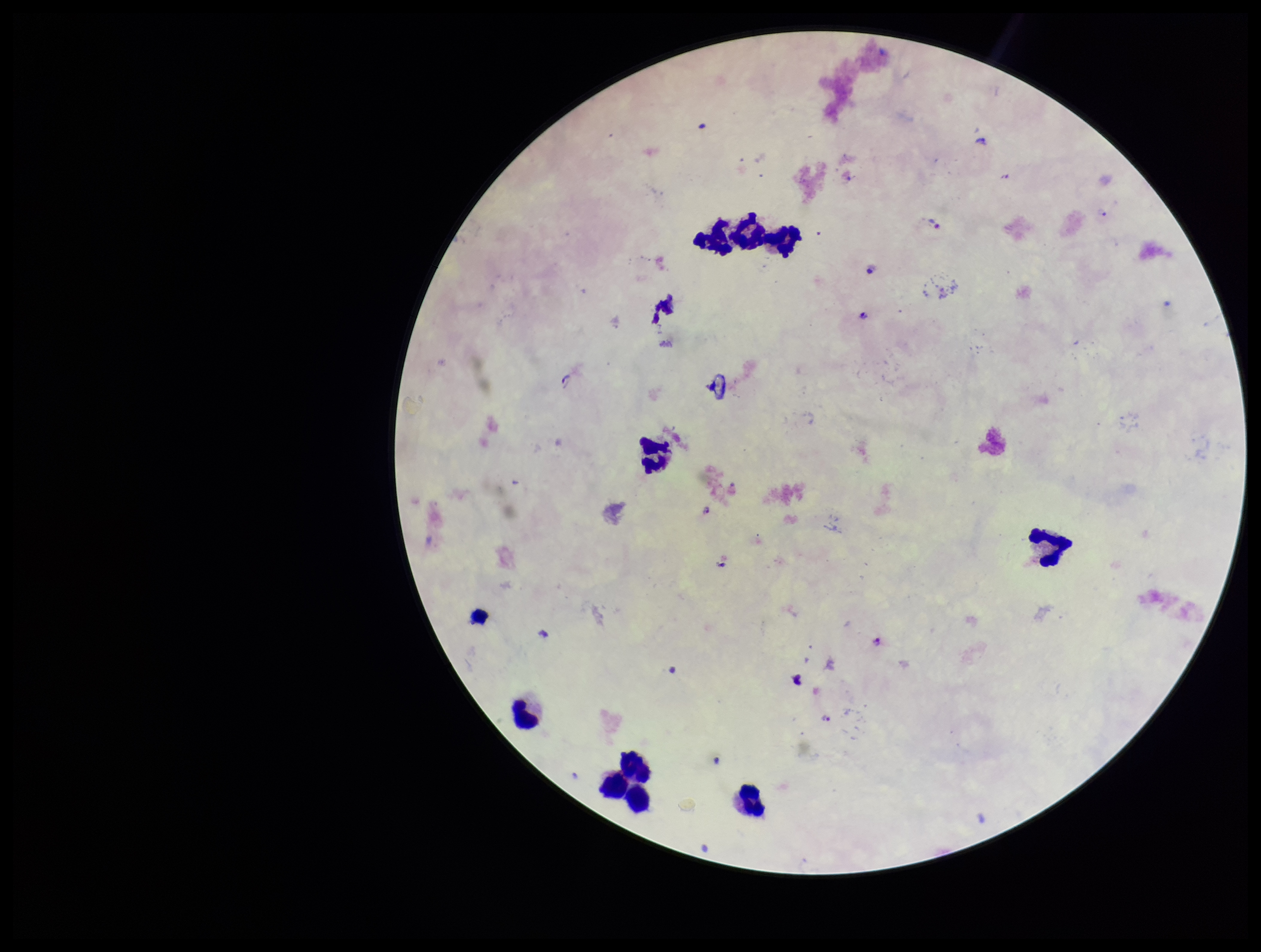

Summary:
  - Stain: Giemsa
  - Capture: smartphone photograph through the microscope eyepiece
  - Plasmodium parasites: detected
  - Species reported for this patient: Plasmodium falciparum
  - Preparation: thick smear
  - Field of view: single
  - Leukocyte count: 10
  - Parasite count: 8
  - Image size: 1261×952 pixels
  - Patient malaria status: infected